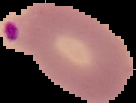 Image is 136×103 pixels. From a thin blood smear. Cell region segmented out of the field of view; the surrounding area is masked to black. Result: malaria parasites identified.